Report the malaria status of this cell.
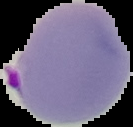

It is parasitized.

Summary:
  - Image size: 133×127 pixels
  - Preparation: thin blood film
  - Image type: cell region segmented out of the field of view; surrounding area masked to black